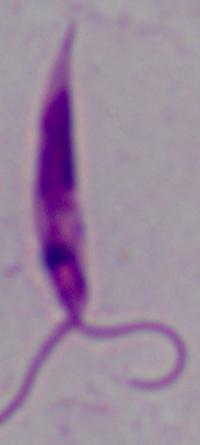

modality = micrograph
identification = Leishmania
magnification = 1000x